Name the blood parasite species.
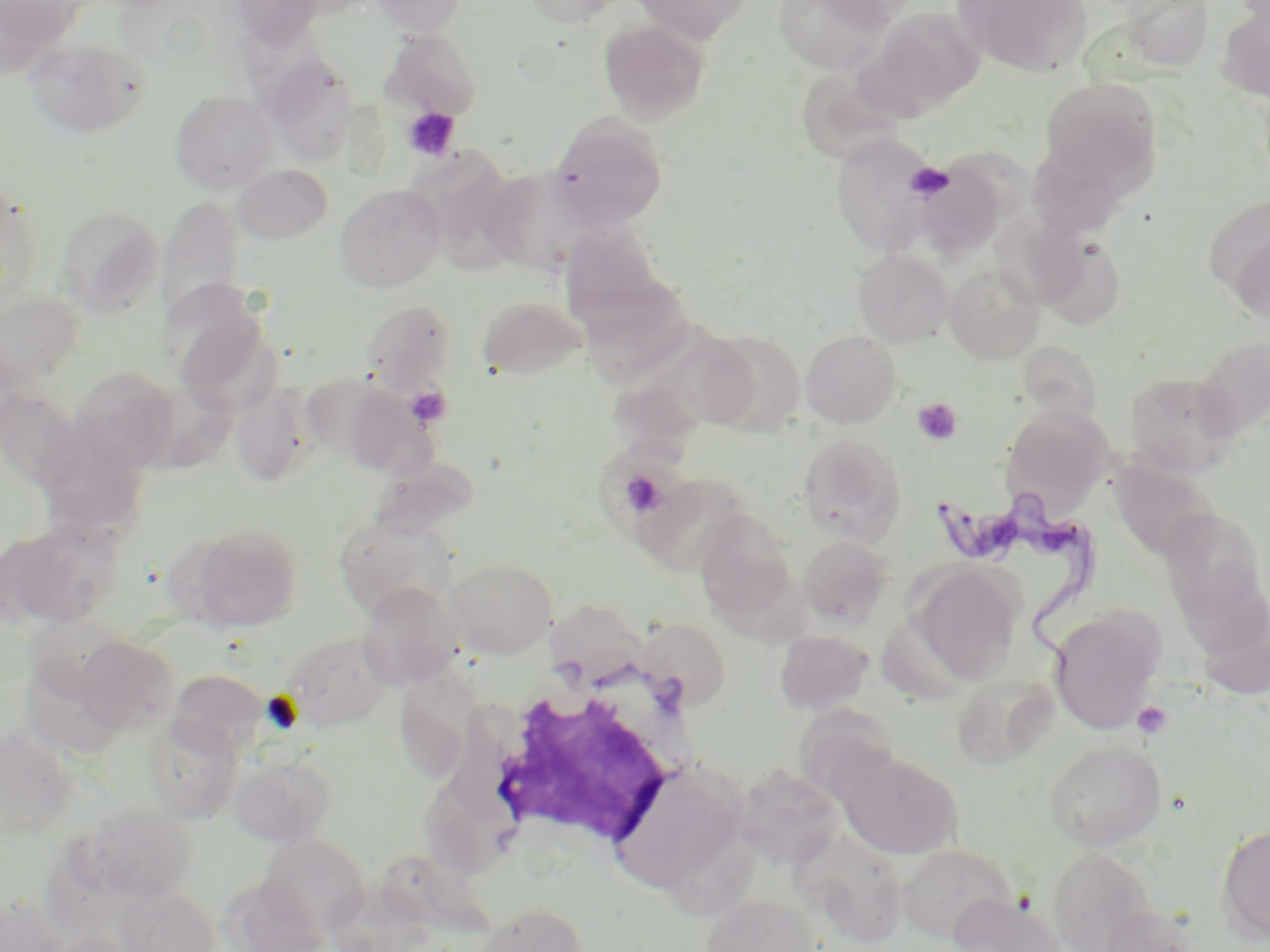
Trypanosoma brucei.

Summary:
  - Coordinate format: approximate bounding boxes as (x1,y1)-(x2,y2) corner pairs in pixels
  - Uninfected red blood cell locations: (232,0)-(326,47), (369,0)-(466,35), (520,0)-(634,27), (629,0)-(753,44), (775,0)-(891,74), (953,0)-(1091,76), (1121,0)-(1214,72), (0,1)-(88,56), (1216,5)-(1270,100), (867,7)-(985,115), (598,20)-(711,125), (382,29)-(482,121), (24,37)-(150,139), (262,53)-(360,164), (798,63)-(913,163), (1038,78)-(1162,193), (170,91)-(279,194), (547,113)-(668,230), (832,133)-(940,257), (1024,143)-(1132,239), (410,147)-(524,273), (911,163)-(1005,261), (233,164)-(333,244), (480,170)-(587,276), (0,184)-(42,310), (334,184)-(445,293), (1203,194)-(1270,304), (163,195)-(246,309), (54,207)-(164,316), (559,222)-(667,325), (1230,224)-(1270,322), (1030,229)-(1127,328), (853,249)-(953,347), (944,264)-(1044,364), (575,272)-(698,385), (161,279)-(270,396), (0,290)-(83,396), (477,295)-(586,380), (360,299)-(456,388), (702,330)-(807,436), (801,330)-(900,427), (1193,337)-(1270,440), (1019,341)-(1108,430), (610,356)-(723,462), (71,367)-(181,471), (1125,371)-(1241,476), (328,380)-(433,477), (125,382)-(237,473), (232,385)-(315,487), (1001,404)-(1114,516), (32,429)-(151,544), (797,435)-(905,545), (369,458)-(479,538), (1111,459)-(1216,560), (635,471)-(756,573), (1160,507)-(1267,625), (693,510)-(802,632), (334,515)-(457,619), (0,524)-(117,631), (188,525)-(302,631), (798,535)-(894,627), (446,557)-(558,657), (910,562)-(1022,683), (357,582)-(463,689), (1195,584)-(1270,701), (541,599)-(658,689), (1048,606)-(1166,734), (635,617)-(731,710), (774,629)-(872,715), (279,632)-(393,731), (74,636)-(179,733), (397,649)-(489,775), (168,668)-(267,754), (950,673)-(1058,770), (796,703)-(899,786), (143,716)-(242,824), (0,729)-(76,837), (1044,740)-(1167,850), (839,752)-(962,859), (229,753)-(335,847), (611,757)-(748,893), (734,764)-(843,868), (423,766)-(535,877), (82,804)-(197,901), (1216,824)-(1270,943), (792,829)-(907,946), (259,834)-(371,935), (896,844)-(1017,943), (1046,847)-(1155,951), (220,876)-(329,952), (115,885)-(220,952), (948,893)-(1065,952), (700,894)-(821,952), (0,895)-(67,952), (476,903)-(588,952), (1098,904)-(1199,952), (42,932)-(138,952)
  - White blood cell locations: (486,669)-(691,847)
  - Trypanosoma brucei locations: (935,484)-(1108,683)
  - Platelet locations: (403,107)-(460,161), (904,162)-(954,201), (406,386)-(451,426), (912,398)-(963,445), (621,469)-(669,516), (1132,700)-(1173,740)
  - Modality: optical microscopy
  - Stain: May-Grünwald-Giemsa
  - Magnification: 1000x
  - Image size: 1270×952 pixels
  - Field of view: one of a larger specimen
  - Preparation: thin blood film